Identify the parasite.
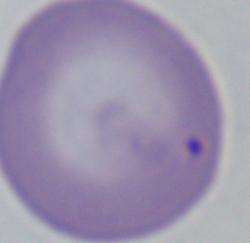

This is Babesia.

{
  "magnification": "1000x",
  "modality": "photomicrograph"
}